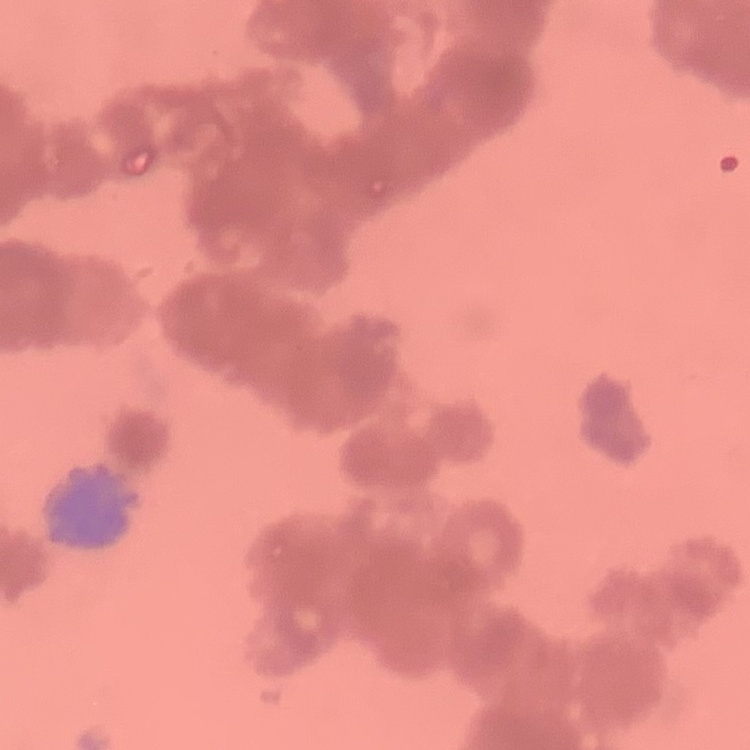

red blood cell morphology = rouleaux formation
image type = square crop of a larger photomicrograph
preparation = thin blood smear
stain = Field's or Giemsa